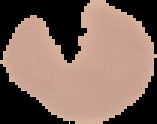

preparation = thin blood film
image type = cell region segmented out of the field of view; surrounding area masked to black
malaria status = parasitized
image size = 157×124 pixels